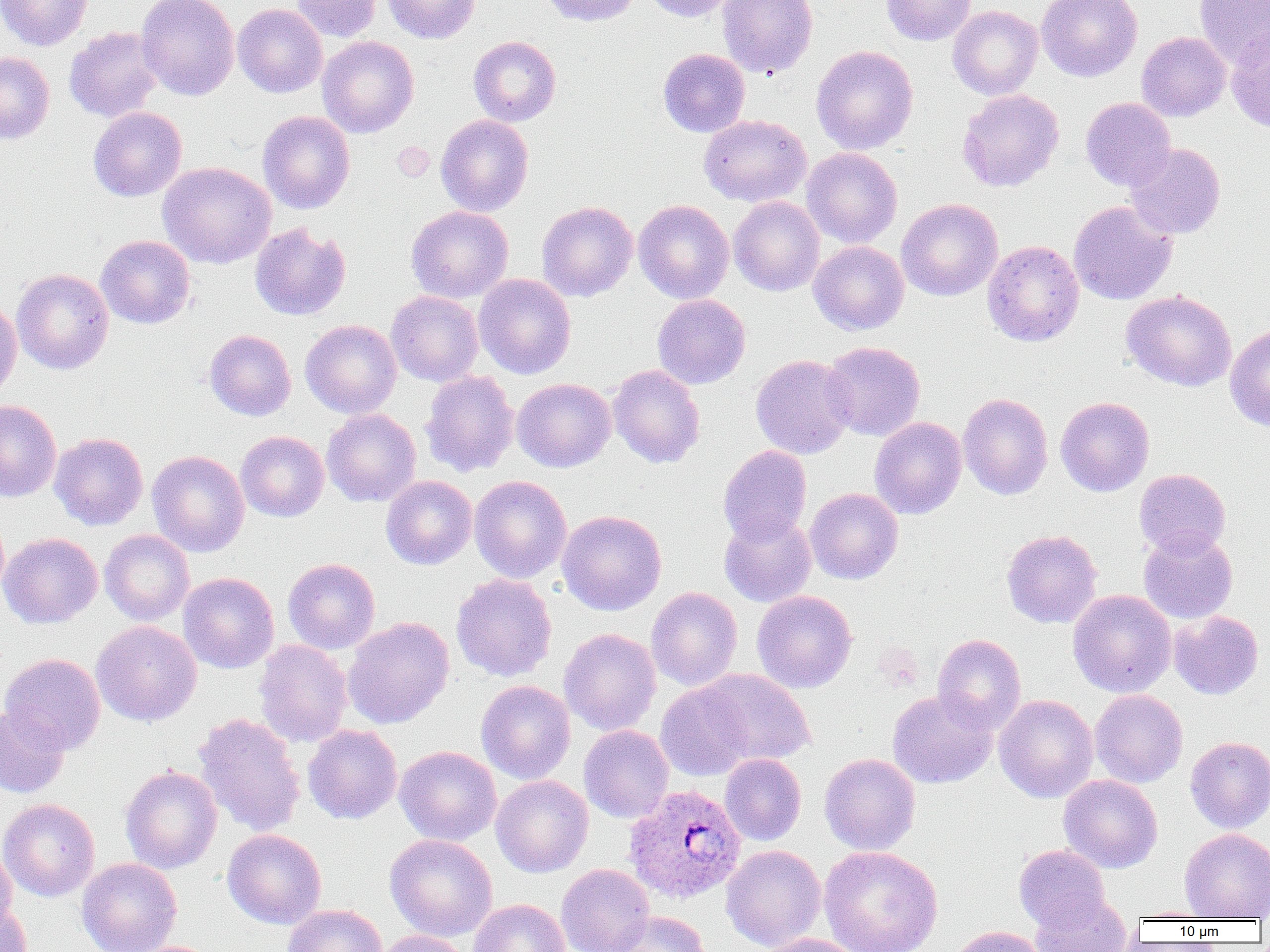

{
  "slide_level_diagnosis": "Plasmodium ovale",
  "field_of_view": "single",
  "uninfected_red_blood_cell_locations_subset": "approximate bounding boxes as (x1, y1, x2, y2) in pixels: (0, 0, 93, 51), (136, 0, 240, 100), (292, 0, 382, 42), (382, 0, 480, 43), (539, 0, 641, 27), (641, 0, 740, 22), (717, 0, 818, 78), (881, 0, 976, 45), (1037, 0, 1142, 82), (1194, 0, 1270, 67), (232, 3, 328, 98), (947, 5, 1043, 100), (64, 26, 164, 123), (1226, 30, 1270, 133), (1136, 31, 1231, 121), (317, 35, 420, 138), (468, 36, 561, 126), (811, 45, 918, 154), (658, 48, 750, 137), (0, 52, 55, 144), (957, 89, 1064, 193), (1080, 97, 1176, 192), (88, 106, 187, 201), (257, 111, 355, 214), (435, 114, 534, 217), (698, 115, 811, 207), (1125, 143, 1226, 240), (802, 147, 902, 248), (157, 162, 277, 269), (728, 196, 825, 296), (633, 199, 734, 304), (896, 199, 1003, 301), (536, 201, 638, 302), (1069, 201, 1178, 305), (406, 205, 514, 303), (249, 222, 350, 320), (96, 234, 195, 329), (982, 240, 1084, 347), (808, 241, 909, 335), (11, 268, 114, 374), (474, 273, 576, 379), (1120, 289, 1237, 391), (386, 291, 484, 386), (652, 294, 751, 389), (0, 295, 22, 403), (300, 319, 402, 418), (1225, 324, 1270, 431), (204, 329, 296, 421), (822, 341, 925, 440), (750, 354, 855, 459), (607, 364, 705, 468), (421, 370, 520, 478), (512, 378, 616, 472), (958, 393, 1053, 500), (1055, 396, 1154, 497), (0, 399, 62, 502), (322, 408, 421, 507), (869, 416, 967, 519), (235, 431, 329, 522), (49, 432, 149, 530), (50, 441, 247, 539), (718, 445, 812, 546), (147, 450, 249, 557), (1134, 468, 1231, 557), (381, 475, 477, 570), (469, 475, 572, 583), (805, 487, 904, 584), (556, 510, 667, 615), (0, 511, 9, 600), (719, 512, 817, 607), (99, 529, 195, 625), (1001, 529, 1102, 628), (1138, 529, 1238, 624), (0, 532, 102, 628), (283, 558, 380, 654), (178, 572, 279, 674), (451, 573, 557, 681), (646, 587, 742, 691), (1067, 589, 1177, 698), (752, 590, 857, 693), (1168, 610, 1264, 700), (343, 617, 454, 729), (90, 621, 202, 726), (559, 628, 661, 736), (933, 633, 1026, 733), (254, 639, 352, 747), (0, 652, 106, 754), (698, 669, 816, 768), (476, 680, 576, 784), (656, 680, 757, 781), (887, 689, 998, 789), (1090, 690, 1188, 788), (994, 694, 1098, 803), (0, 704, 70, 797), (193, 712, 306, 838), (303, 724, 402, 824), (579, 724, 674, 823), (1185, 736, 1270, 833), (394, 746, 501, 845), (720, 753, 806, 846), (819, 753, 921, 855), (120, 766, 222, 873), (1059, 774, 1163, 873), (490, 775, 593, 878), (0, 798, 100, 901), (222, 828, 327, 929), (1179, 828, 1270, 921), (384, 834, 497, 941), (0, 842, 17, 933), (1013, 844, 1110, 932), (720, 845, 827, 951), (818, 845, 944, 952), (76, 858, 182, 952), (556, 863, 655, 952), (1031, 893, 1133, 952), (469, 898, 569, 952), (0, 900, 33, 952), (283, 904, 387, 952), (1132, 907, 1222, 921), (605, 910, 710, 952), (945, 925, 1048, 952), (375, 930, 472, 952), (756, 933, 867, 952)",
  "image_size": "1270×952 pixels",
  "magnification": "1000x",
  "preparation": "thin blood smear",
  "modality": "light microscopy",
  "plasmodium_ovale_infected_red_blood_cell_locations": "approximate bounding boxes as (x1, y1, x2, y2) in pixels: (623, 783, 746, 903)"
}